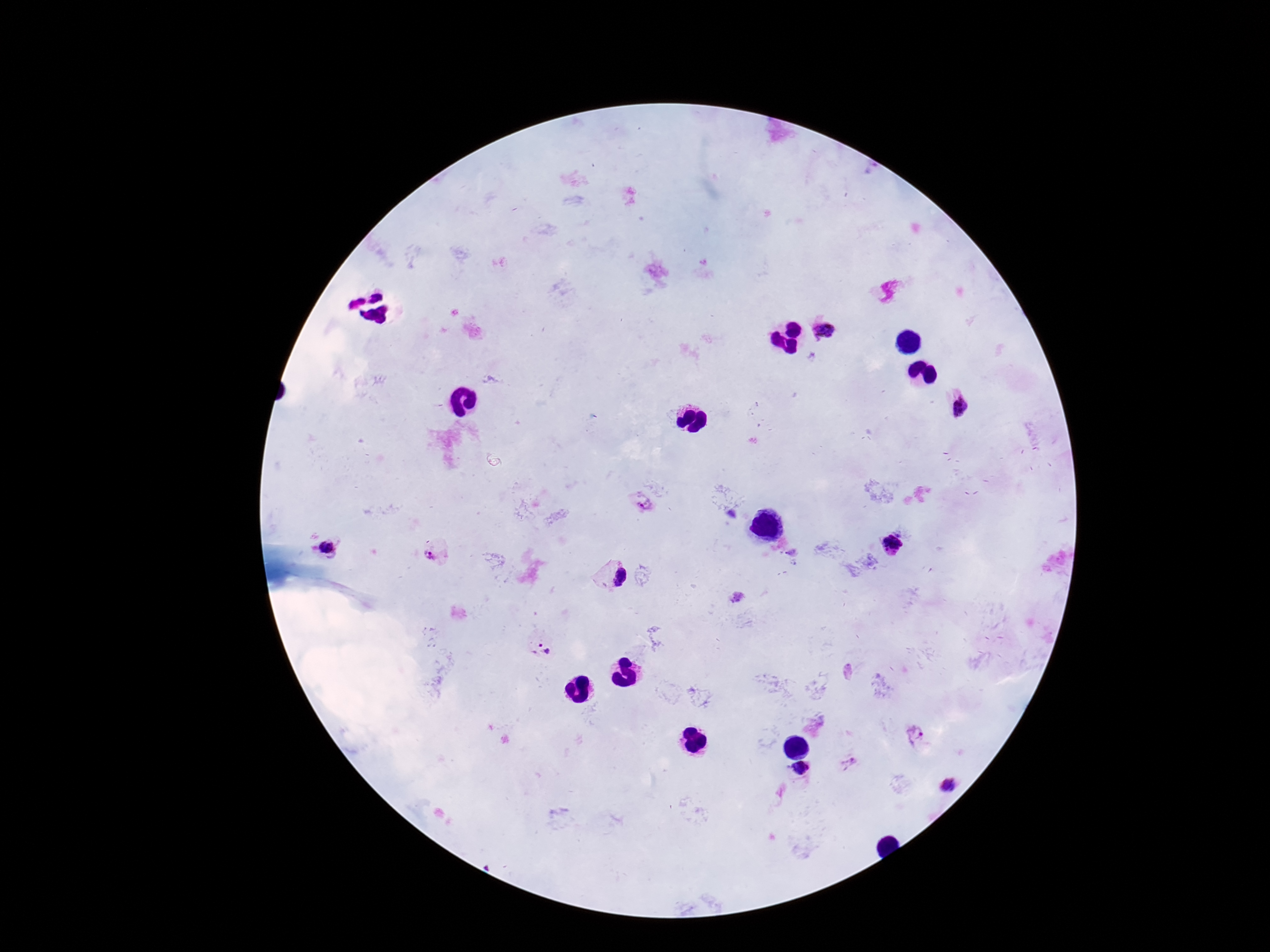

Approximate centers as (x, y) in pixels. Plasmodium parasite locations: (826, 329), (961, 404), (646, 506), (894, 543), (329, 548), (616, 577), (543, 649), (916, 735), (850, 762), (801, 769), (947, 786). Image is 1270×952 pixels. One field from this slide. Photographed through the microscope eyepiece with a smartphone camera. 100x magnification. Patient malaria status: infected. Giemsa-stained preparation. Thick blood smear.